Assess this cell for malaria.
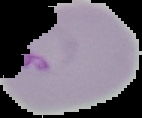
It is parasitized.

Segmented cell region on a black background. Image is 142×118 pixels. From a thin blood film.